Assess this cell for malaria.
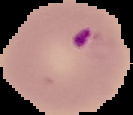

Parasitized.

Summary:
  - Image size: 133×115 pixels
  - Image type: segmented cell region with the area outside set to black
  - Preparation: thin blood film